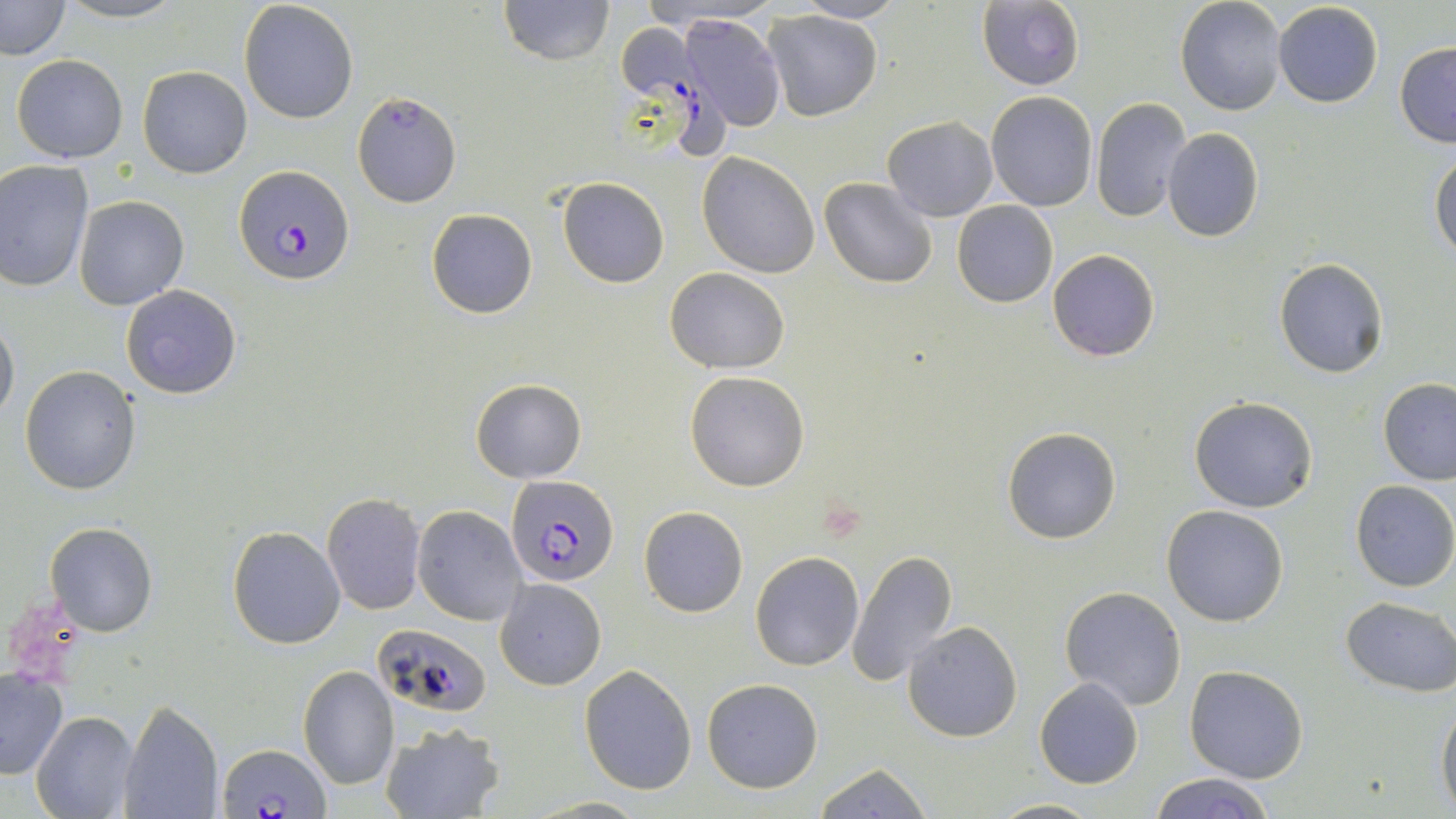
Approximate bounding boxes as (x1,y1)-(x2,y2) corner pairs in pixels. Platelet locations: (4,599)-(83,682). Plasmodium falciparum-infected red blood cell locations: (618,24)-(728,158), (235,165)-(354,285), (506,474)-(619,585), (370,625)-(493,717), (220,742)-(328,817). Uninfected red blood cell locations: (52,0)-(191,25), (497,0)-(615,66), (1175,0)-(1287,115), (1,1)-(71,60), (239,1)-(359,122), (790,1)-(907,24), (976,1)-(1086,90), (1273,2)-(1383,108), (763,10)-(883,121), (680,15)-(786,131), (1394,40)-(1456,147), (11,54)-(128,164), (138,65)-(252,178), (352,91)-(463,209), (987,92)-(1098,211), (1091,97)-(1191,222), (882,115)-(999,221), (1162,128)-(1264,242), (1429,149)-(1456,261), (697,152)-(820,278), (0,160)-(92,292), (557,176)-(670,288), (820,177)-(939,289), (74,195)-(190,311), (952,201)-(1058,307), (426,208)-(539,319), (1047,249)-(1160,362), (1274,258)-(1390,379), (665,267)-(788,374), (119,285)-(243,399), (0,314)-(19,426), (20,366)-(141,496), (684,371)-(810,492), (1377,378)-(1456,485), (470,379)-(587,483), (1189,396)-(1319,514), (1001,425)-(1122,544), (1351,480)-(1456,592), (322,493)-(427,614), (639,505)-(748,618), (1162,505)-(1290,627), (413,506)-(527,625), (46,522)-(158,636), (227,525)-(345,649), (846,550)-(959,690), (750,551)-(864,672), (495,577)-(607,691), (1059,586)-(1187,712), (1341,597)-(1456,696), (904,620)-(1023,742), (298,665)-(401,789), (580,665)-(699,795), (1185,665)-(1309,784), (0,669)-(68,778), (701,677)-(825,793), (1034,678)-(1143,789), (1436,696)-(1456,815), (118,700)-(225,819), (30,710)-(138,819), (379,722)-(506,819), (814,764)-(931,818), (1150,772)-(1274,819), (988,797)-(1101,817). Slide-level diagnosis: Plasmodium falciparum. Light microscopy. May-Grünwald-Giemsa stain. Image is 1456×819 pixels. Thin blood film. 1000x magnification. Single field of view.